Locate every blood parasite and identify its species.
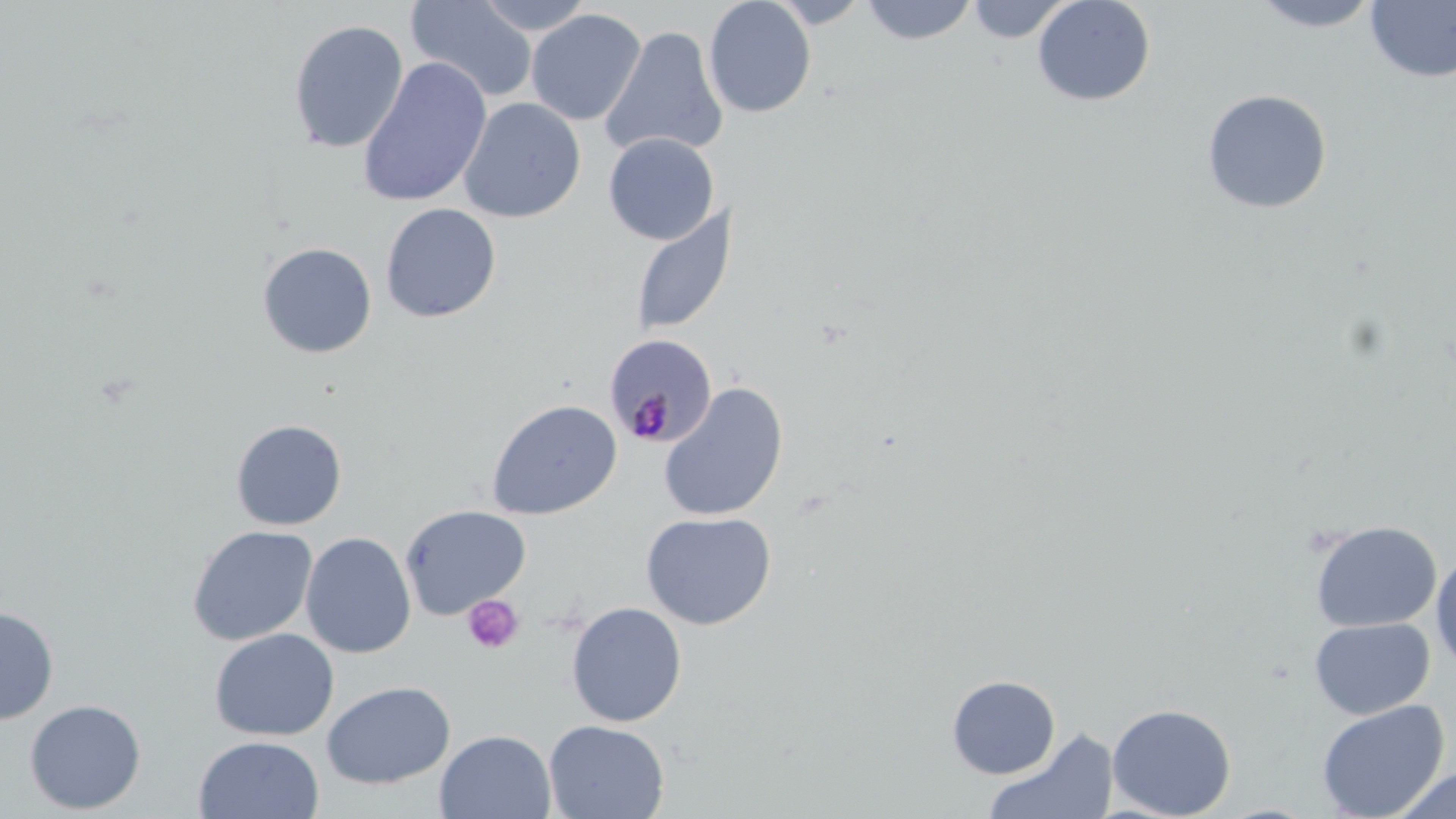

Approximate bounding boxes as named x1/y1/x2/y2 corners in pixels.
Plasmodium malariae-infected red blood cells: (x1=603, y1=333, x2=718, y2=448).
No Plasmodium falciparum, Plasmodium ovale, Plasmodium vivax, Babesia divergens, or Trypanosoma brucei observed.

Platelet locations: (x1=462, y1=594, x2=524, y2=654). Uninfected red blood cell locations: (x1=405, y1=0, x2=538, y2=104), (x1=473, y1=0, x2=596, y2=35), (x1=703, y1=0, x2=817, y2=118), (x1=765, y1=0, x2=874, y2=29), (x1=860, y1=0, x2=979, y2=45), (x1=965, y1=0, x2=1074, y2=43), (x1=1032, y1=0, x2=1156, y2=107), (x1=1246, y1=0, x2=1385, y2=33), (x1=1365, y1=1, x2=1456, y2=83), (x1=526, y1=9, x2=646, y2=126), (x1=288, y1=19, x2=409, y2=154), (x1=599, y1=26, x2=727, y2=160), (x1=357, y1=57, x2=492, y2=208), (x1=1201, y1=89, x2=1332, y2=214), (x1=459, y1=97, x2=586, y2=223), (x1=603, y1=133, x2=719, y2=245), (x1=379, y1=202, x2=501, y2=323), (x1=630, y1=204, x2=737, y2=337), (x1=257, y1=242, x2=377, y2=359), (x1=657, y1=381, x2=789, y2=522), (x1=486, y1=399, x2=622, y2=520), (x1=230, y1=419, x2=347, y2=530), (x1=400, y1=504, x2=531, y2=618), (x1=640, y1=510, x2=777, y2=630), (x1=1310, y1=520, x2=1442, y2=632), (x1=186, y1=525, x2=318, y2=646), (x1=300, y1=532, x2=416, y2=658), (x1=1430, y1=548, x2=1456, y2=674), (x1=566, y1=601, x2=687, y2=727), (x1=0, y1=606, x2=59, y2=724), (x1=1309, y1=617, x2=1435, y2=720), (x1=209, y1=628, x2=338, y2=741), (x1=946, y1=674, x2=1062, y2=779), (x1=321, y1=680, x2=455, y2=789), (x1=24, y1=699, x2=145, y2=814), (x1=1316, y1=699, x2=1450, y2=818), (x1=1107, y1=702, x2=1237, y2=819), (x1=544, y1=720, x2=670, y2=818), (x1=982, y1=727, x2=1119, y2=819), (x1=435, y1=729, x2=556, y2=819), (x1=193, y1=734, x2=324, y2=819), (x1=1388, y1=766, x2=1456, y2=818). Slide-level diagnosis: Plasmodium malariae. Captured at 1000x magnification. One field of a larger specimen. May-Grünwald-Giemsa-stained preparation. Image is 1456×819 pixels. Optical microscopy. Thin blood film.